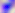

identification: Toxoplasma gondii
magnification: 400x
modality: photomicrograph